Name the parasite shown.
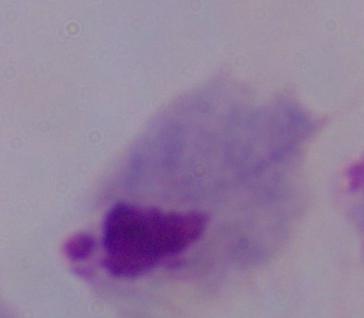

A trichomonad.

Summary:
  - Modality: photomicrograph
  - Magnification: 1000x